Give the preparation type.
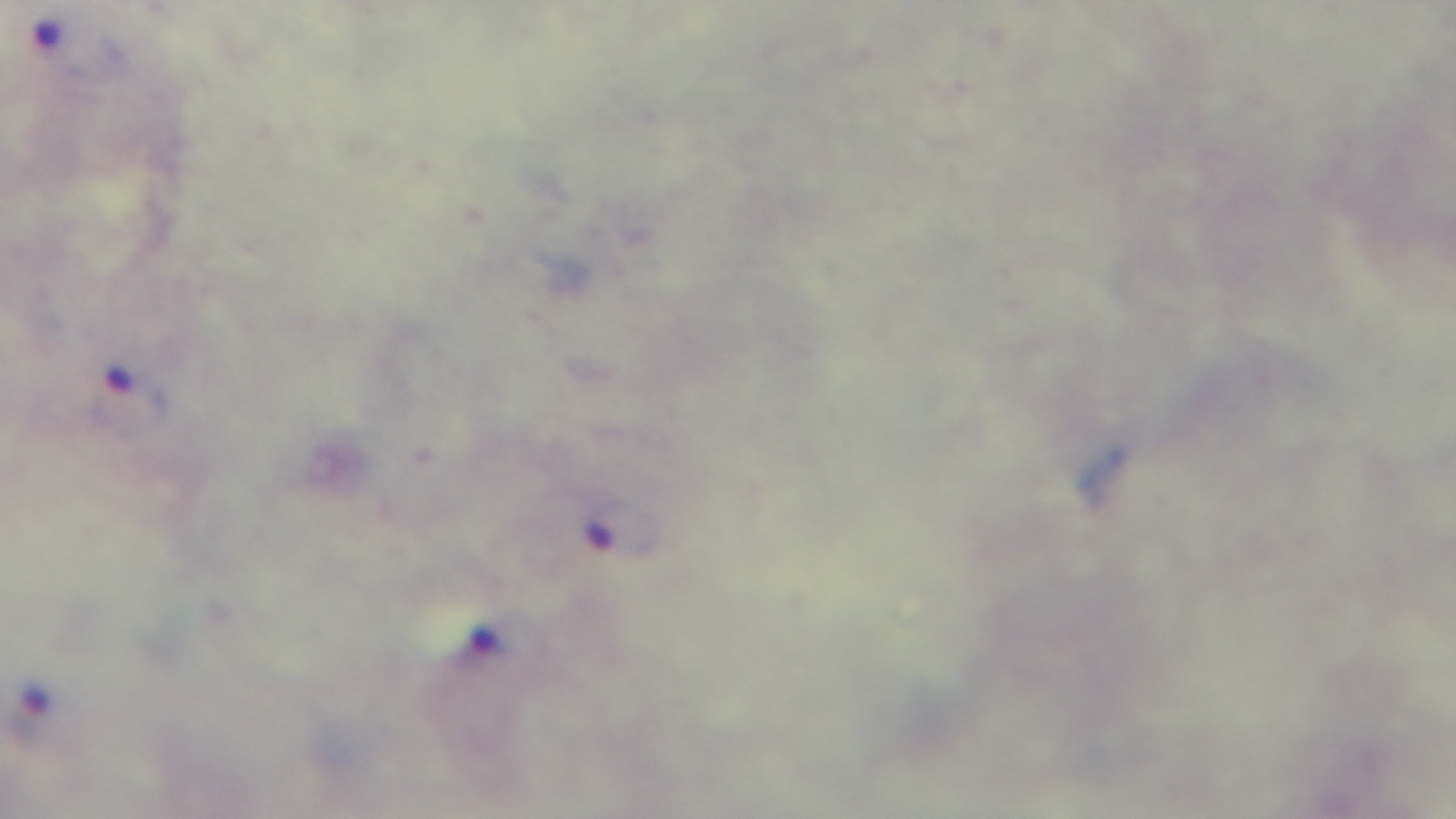

It is a thick blood film.

capture: mounted 4K digital camera
modality: light microscopy
stain: Giemsa
objective: 100x oil immersion
malaria_status: positive
field_of_view: single